Comment on the morphology of the red blood cells.
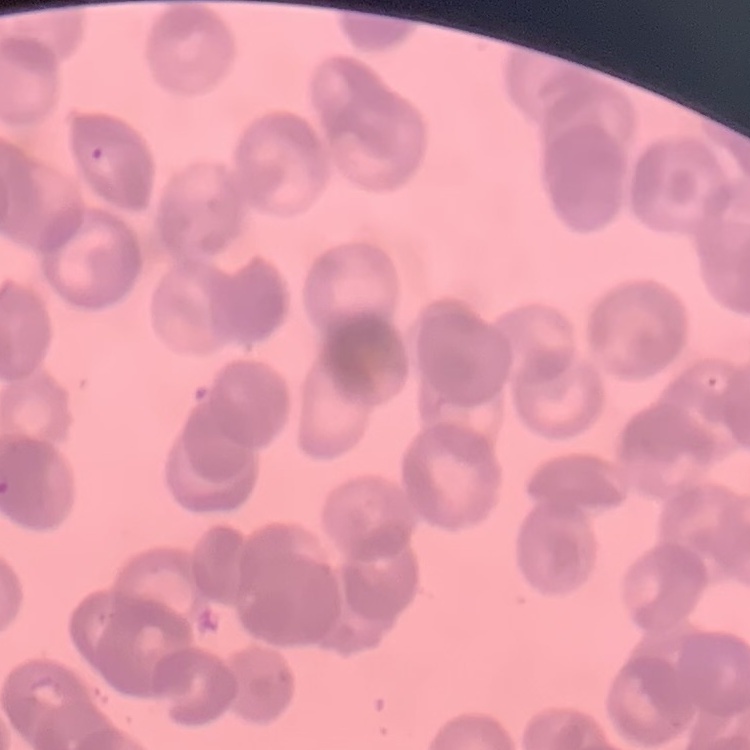

They show rouleaux formation.

image type = square crop of a larger photomicrograph
stain = Field's or Giemsa
preparation = thin blood smear